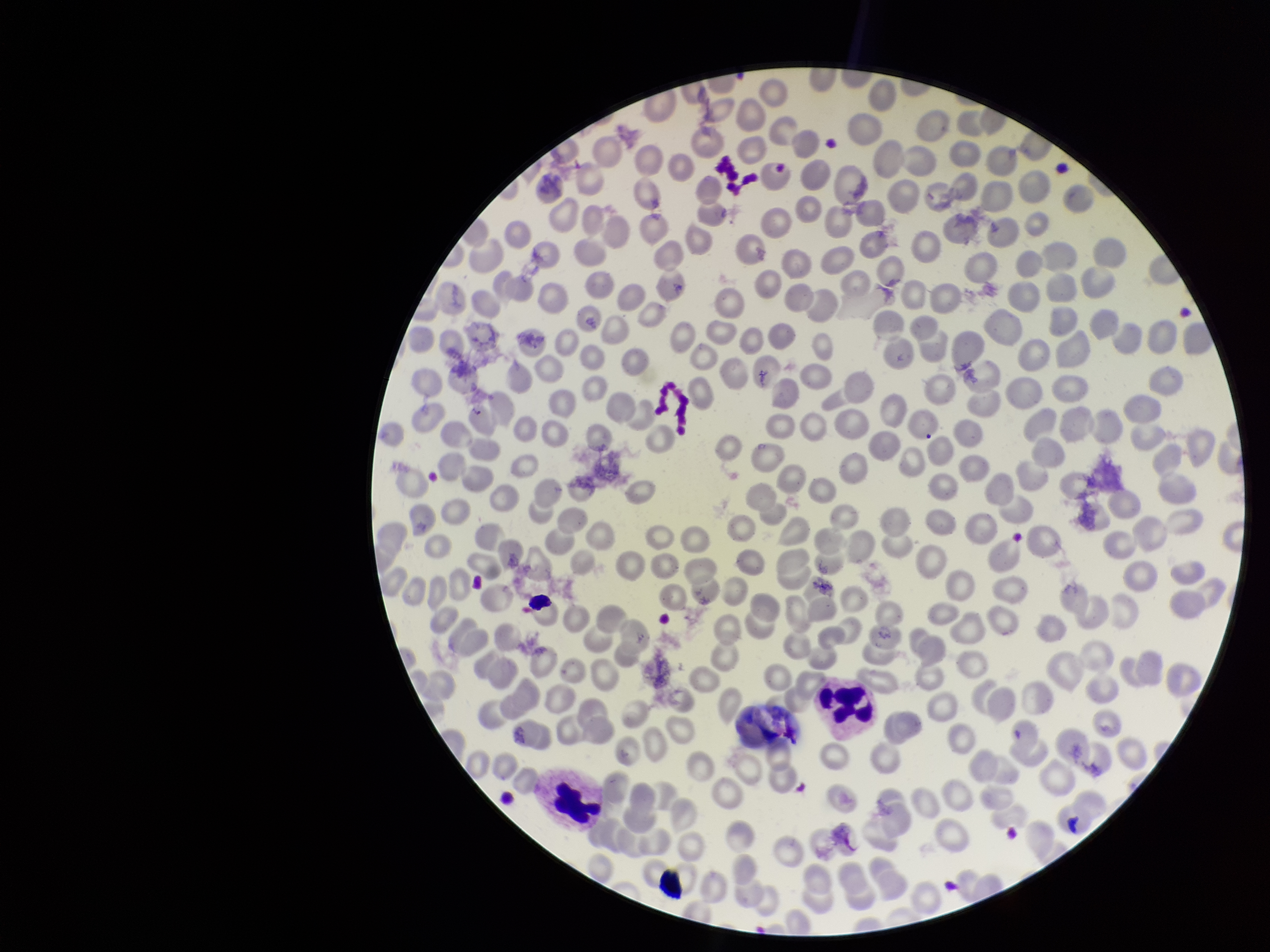 Photographed through the microscope eyepiece with a smartphone camera. Parasitized red blood cell count: 0. Stained with Giemsa. Patient malaria status: negative. Parasitized red blood cells: none identified. Single field of view. Red blood cell count: 289. Image is 1270×952 pixels. Preparation: thin.